Report the malaria status of this cell.
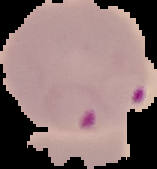
It is parasitized.

From a thin blood smear. Segmented cell region on a black background. Image is 157×169 pixels.